Report the malaria status of this cell.
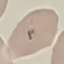

Uninfected.

Summary:
  - Preparation: thin smear
  - Image type: cell patch, automatically extracted from a larger field of view and resized to 64 × 64 pixels
  - Stain: Giemsa
  - Capture: smartphone camera at the microscope eyepiece